State the blood parasite species.
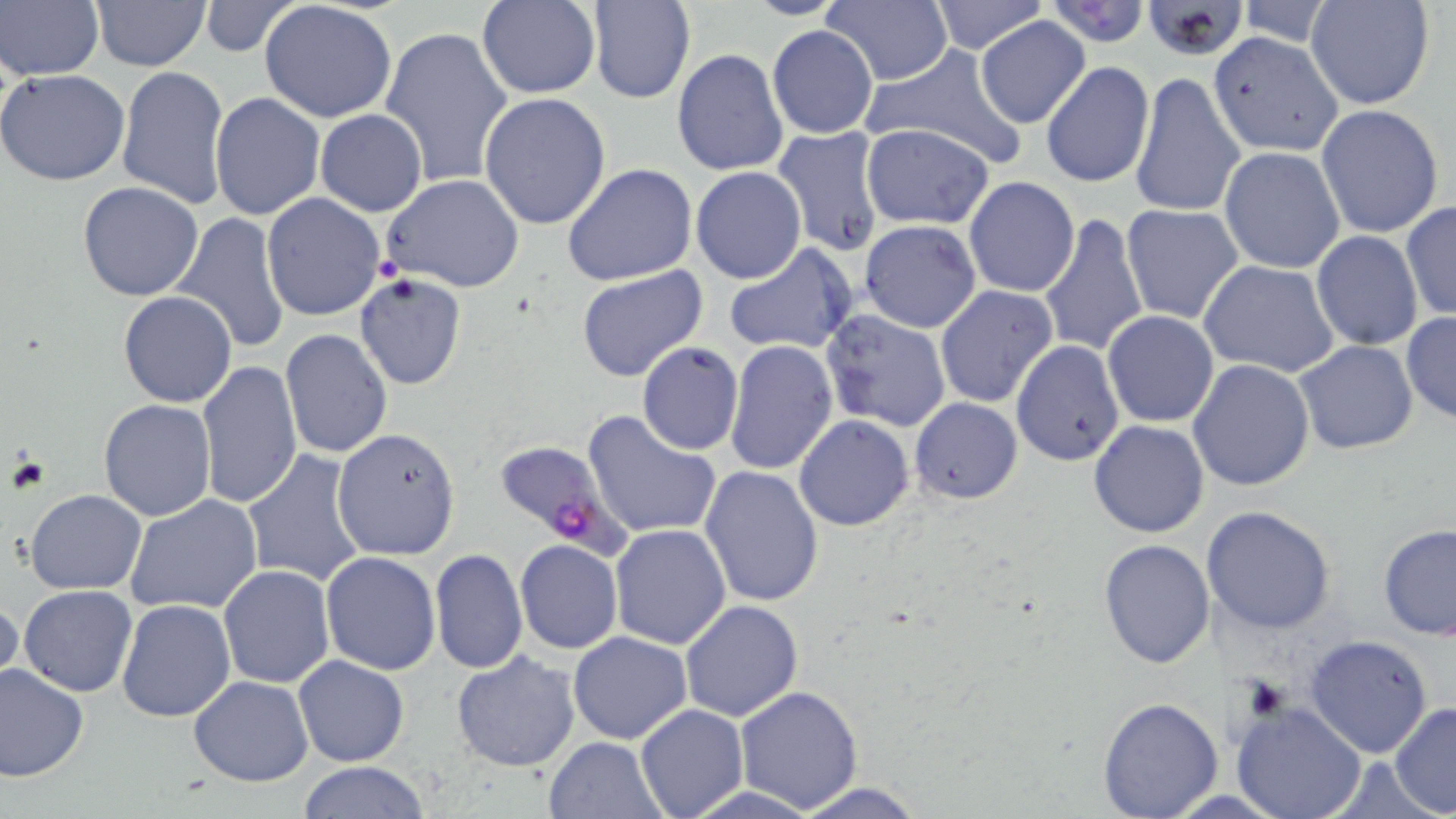
Plasmodium falciparum.

stain = May-Grünwald-Giemsa
preparation = thin blood smear
field of view = single
image size = 1456×819 pixels
Plasmodium falciparum-infected red blood cell locations = approximate bounding boxes as named x1/y1/x2/y2 corners in pixels: (x1=489, y1=437, x2=628, y2=554)
uninfected red blood cell locations = approximate bounding boxes as named x1/y1/x2/y2 corners in pixels: (x1=2, y1=0, x2=102, y2=83), (x1=90, y1=0, x2=212, y2=71), (x1=476, y1=0, x2=600, y2=100), (x1=739, y1=0, x2=850, y2=20), (x1=928, y1=0, x2=1047, y2=54), (x1=1139, y1=0, x2=1254, y2=60), (x1=259, y1=1, x2=397, y2=123), (x1=586, y1=1, x2=694, y2=104), (x1=1040, y1=1, x2=1155, y2=47), (x1=1305, y1=1, x2=1435, y2=110), (x1=197, y1=2, x2=302, y2=57), (x1=823, y1=2, x2=953, y2=85), (x1=1230, y1=2, x2=1339, y2=45), (x1=977, y1=15, x2=1090, y2=127), (x1=379, y1=24, x2=514, y2=189), (x1=767, y1=24, x2=879, y2=139), (x1=1211, y1=34, x2=1340, y2=155), (x1=862, y1=45, x2=1028, y2=168), (x1=672, y1=47, x2=790, y2=178), (x1=1040, y1=61, x2=1156, y2=189), (x1=116, y1=66, x2=232, y2=209), (x1=0, y1=69, x2=131, y2=186), (x1=1133, y1=70, x2=1246, y2=220), (x1=478, y1=91, x2=612, y2=231), (x1=208, y1=92, x2=325, y2=221), (x1=1316, y1=104, x2=1445, y2=238), (x1=315, y1=108, x2=427, y2=217), (x1=861, y1=124, x2=995, y2=230), (x1=772, y1=126, x2=885, y2=256), (x1=1219, y1=147, x2=1346, y2=272), (x1=562, y1=162, x2=698, y2=285), (x1=691, y1=166, x2=807, y2=284), (x1=380, y1=173, x2=525, y2=294), (x1=964, y1=177, x2=1080, y2=297), (x1=76, y1=182, x2=205, y2=301), (x1=987, y1=185, x2=1136, y2=323), (x1=260, y1=193, x2=386, y2=321), (x1=1400, y1=201, x2=1456, y2=323), (x1=1120, y1=203, x2=1245, y2=324), (x1=1037, y1=210, x2=1149, y2=359), (x1=171, y1=211, x2=291, y2=354), (x1=858, y1=219, x2=982, y2=333), (x1=1311, y1=230, x2=1424, y2=351), (x1=723, y1=243, x2=858, y2=356), (x1=1199, y1=260, x2=1340, y2=380), (x1=576, y1=265, x2=708, y2=382), (x1=355, y1=275, x2=467, y2=390), (x1=934, y1=285, x2=1059, y2=408), (x1=118, y1=292, x2=237, y2=408), (x1=820, y1=307, x2=951, y2=432), (x1=1102, y1=310, x2=1219, y2=427), (x1=1400, y1=313, x2=1456, y2=423), (x1=279, y1=330, x2=393, y2=461), (x1=724, y1=340, x2=838, y2=474), (x1=1293, y1=340, x2=1418, y2=455), (x1=637, y1=341, x2=744, y2=455), (x1=1011, y1=341, x2=1124, y2=467), (x1=1188, y1=359, x2=1315, y2=490), (x1=195, y1=361, x2=301, y2=511), (x1=909, y1=397, x2=1022, y2=504), (x1=99, y1=399, x2=215, y2=520), (x1=582, y1=409, x2=724, y2=539), (x1=795, y1=415, x2=913, y2=531), (x1=1087, y1=419, x2=1210, y2=538), (x1=332, y1=427, x2=460, y2=562), (x1=242, y1=449, x2=368, y2=588), (x1=699, y1=464, x2=825, y2=609), (x1=25, y1=489, x2=146, y2=594), (x1=124, y1=494, x2=264, y2=614), (x1=1202, y1=505, x2=1335, y2=633), (x1=1377, y1=522, x2=1456, y2=640), (x1=608, y1=524, x2=731, y2=648), (x1=1098, y1=539, x2=1216, y2=668), (x1=515, y1=540, x2=622, y2=653), (x1=430, y1=548, x2=526, y2=675), (x1=320, y1=552, x2=442, y2=675), (x1=218, y1=565, x2=335, y2=688), (x1=19, y1=585, x2=137, y2=697), (x1=0, y1=597, x2=24, y2=701), (x1=116, y1=598, x2=236, y2=721), (x1=678, y1=599, x2=803, y2=720), (x1=568, y1=632, x2=692, y2=744), (x1=1303, y1=635, x2=1435, y2=758), (x1=450, y1=650, x2=582, y2=772), (x1=293, y1=655, x2=410, y2=767), (x1=0, y1=663, x2=89, y2=782), (x1=188, y1=676, x2=312, y2=786), (x1=733, y1=685, x2=864, y2=812), (x1=1096, y1=697, x2=1223, y2=817), (x1=1229, y1=700, x2=1369, y2=819), (x1=1390, y1=702, x2=1456, y2=817), (x1=635, y1=704, x2=748, y2=818), (x1=543, y1=735, x2=666, y2=818), (x1=296, y1=762, x2=432, y2=818), (x1=786, y1=780, x2=931, y2=818)
magnification = 1000x
platelet locations = approximate bounding boxes as named x1/y1/x2/y2 corners in pixels: (x1=370, y1=250, x2=405, y2=288)
modality = optical microscopy